Comment on the morphology of the red blood cells.
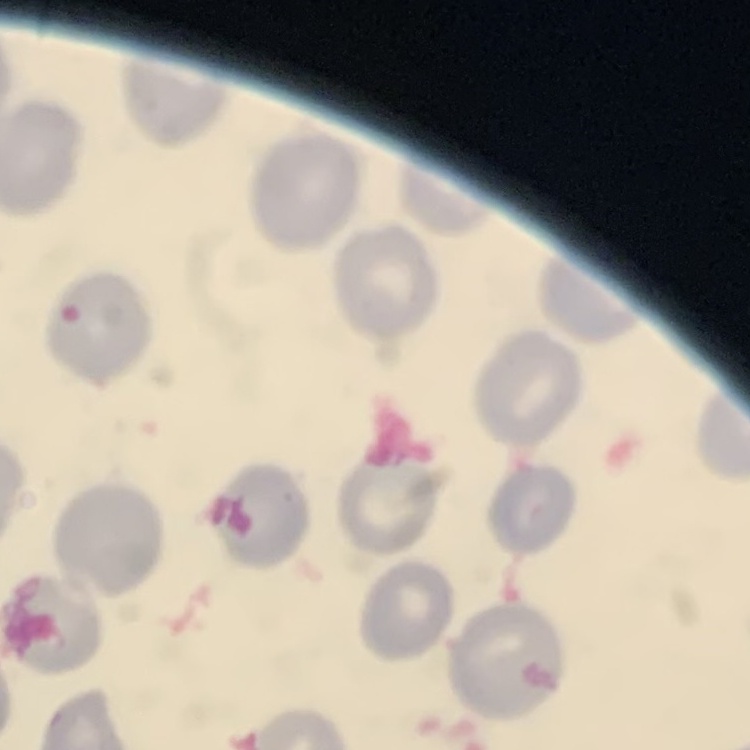
They show no rouleaux formation.

image type = square crop of a larger photomicrograph
stain = Field's or Giemsa
preparation = thin blood film